Give the extent of all white blood cells.
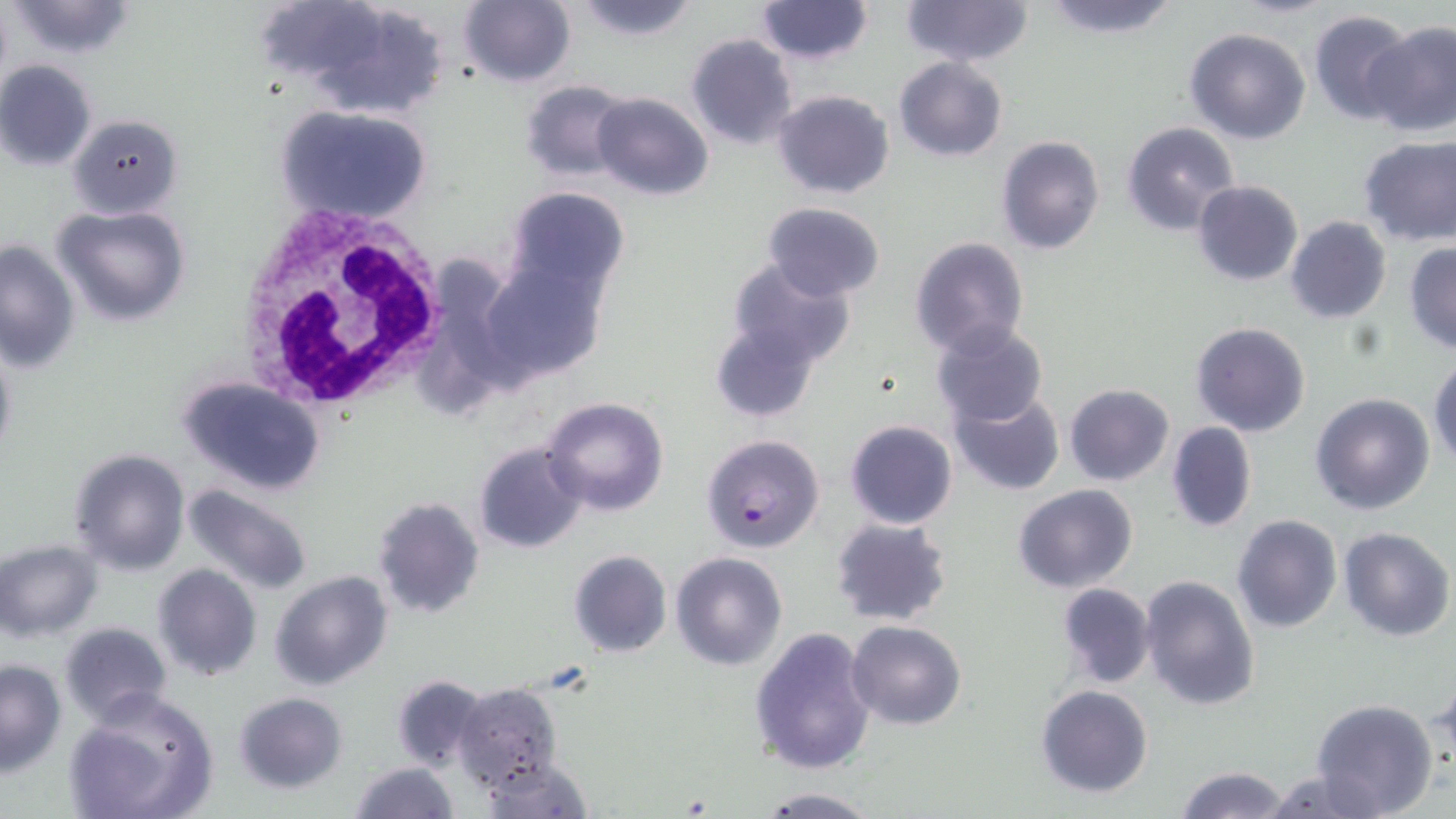
Approximate bounding boxes as (x1,y1)-(x2,y2) corner pairs in pixels.
White blood cells: (230,202)-(452,415).

Summary:
  - Plasmodium falciparum-infected red blood cell locations: (700,433)-(825,552)
  - Uninfected red blood cell locations: (6,0)-(137,59), (459,0)-(574,86), (569,0)-(700,41), (901,0)-(1032,68), (1038,0)-(1182,38), (756,1)-(871,64), (1307,10)-(1415,124), (1359,21)-(1456,136), (1184,28)-(1312,146), (686,34)-(796,150), (894,56)-(1006,162), (0,61)-(98,170), (518,79)-(633,181), (771,89)-(895,200), (592,92)-(712,201), (276,105)-(433,224), (68,113)-(183,217), (1120,122)-(1239,236), (996,136)-(1106,256), (1357,136)-(1456,247), (1192,179)-(1304,286), (506,186)-(629,299), (763,201)-(884,301), (50,204)-(192,327), (1284,216)-(1392,323), (909,237)-(1030,358), (0,238)-(81,375), (1403,242)-(1456,353), (722,257)-(856,372), (480,258)-(604,384), (709,309)-(831,423), (1190,321)-(1311,437), (932,324)-(1049,428), (0,332)-(18,472), (1429,358)-(1456,470), (177,376)-(327,495), (1063,382)-(1174,487), (1310,392)-(1437,515), (949,393)-(1066,495), (541,396)-(670,517), (844,419)-(958,530), (1166,421)-(1257,532), (473,441)-(587,554), (68,447)-(192,575), (181,483)-(313,598), (1013,484)-(1137,594), (371,497)-(485,619), (1231,515)-(1342,635), (830,516)-(954,628), (1338,527)-(1454,641), (0,540)-(102,641), (568,550)-(671,658), (670,551)-(788,670), (151,563)-(263,682), (269,570)-(394,691), (1138,575)-(1260,711), (1055,582)-(1155,689), (846,620)-(966,730), (58,621)-(173,727), (749,627)-(877,775), (0,659)-(66,774), (1428,672)-(1455,776), (389,673)-(488,772), (452,682)-(563,791), (1034,684)-(1155,799), (62,689)-(221,819), (232,691)-(347,793), (1309,699)-(1439,819), (477,755)-(592,817), (348,762)-(459,818), (1173,764)-(1290,819), (1263,767)-(1388,819), (753,788)-(882,817)
  - Slide-level diagnosis: Plasmodium falciparum
  - Stain: May-Grünwald-Giemsa
  - Modality: optical microscopy
  - Magnification: 1000x
  - Preparation: thin blood film
  - Image size: 1456×819 pixels
  - Field of view: single